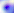
Micrograph. Toxoplasma gondii is seen. 400x magnification.